Report the malaria status of this cell.
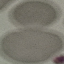

Uninfected.

Giemsa-stained preparation. Thin smear of blood. Acquired by smartphone through the microscope eyepiece. Automatically extracted cell patch, resized to 64 × 64 pixels.